Comment on the morphology of the erythrocytes.
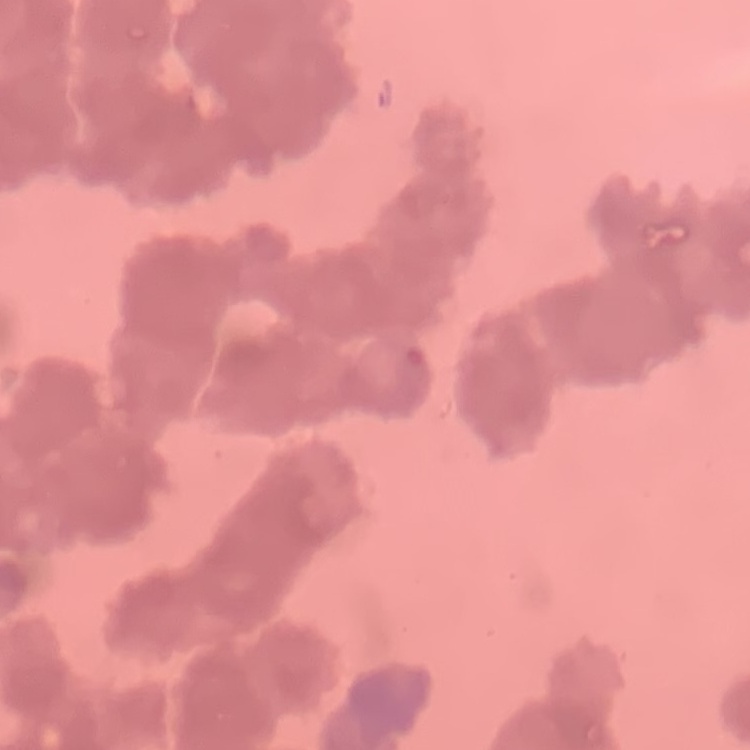

Rouleaux formation.

Square crop of a larger photomicrograph. Field's or Giemsa stain. Thin blood smear.